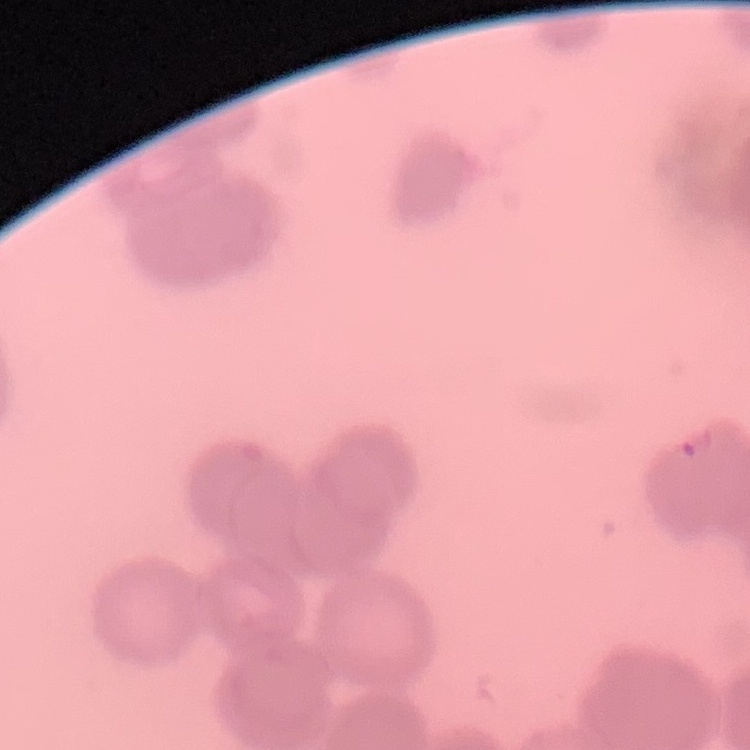
The red blood cells exhibit rouleaux formation. Stained with either Field's or Giemsa. Thin blood film. Square crop of a larger photomicrograph.